Assess this cell for malaria.
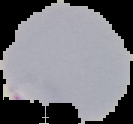
Parasitized.

From a thin blood film. Cell region segmented out of the field of view; the surrounding area is masked to black. Image is 133×124 pixels.